Locate and identify every blood parasite.
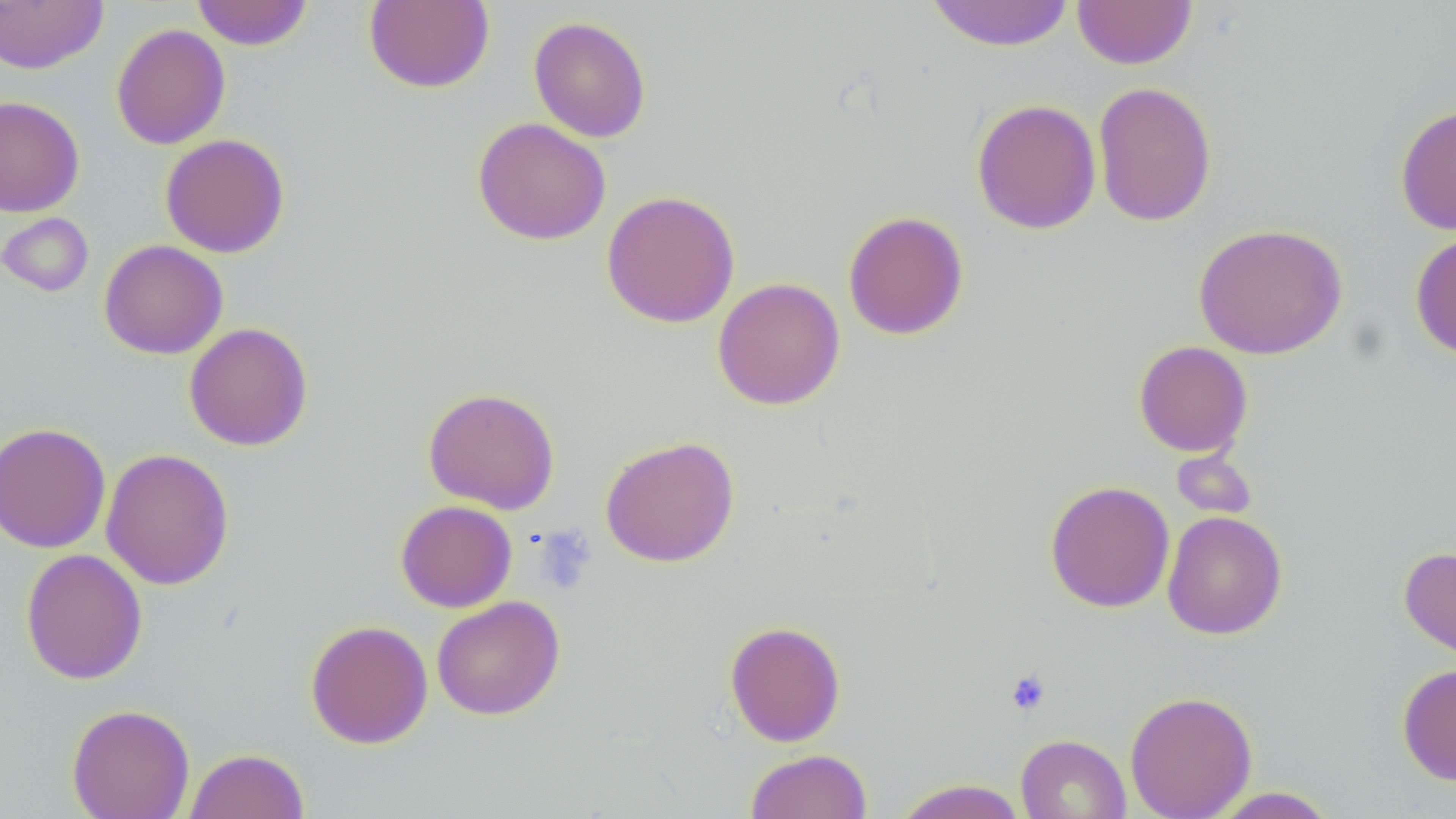

No blood parasites observed.

slide-level diagnosis = no evidence of blood parasites
field of view = single
stain = May-Grünwald-Giemsa
modality = optical microscopy
platelet locations = approximate bounding boxes as named x1/y1/x2/y2 corners in pixels: (x1=1005, y1=671, x2=1051, y2=715)
preparation = thin blood smear
uninfected red blood cell locations = approximate bounding boxes as named x1/y1/x2/y2 corners in pixels: (x1=191, y1=0, x2=313, y2=50), (x1=1072, y1=0, x2=1197, y2=70), (x1=0, y1=1, x2=108, y2=74), (x1=364, y1=1, x2=495, y2=93), (x1=926, y1=1, x2=1075, y2=52), (x1=529, y1=16, x2=652, y2=143), (x1=111, y1=23, x2=231, y2=150), (x1=1093, y1=81, x2=1217, y2=228), (x1=0, y1=95, x2=85, y2=217), (x1=971, y1=98, x2=1101, y2=235), (x1=1394, y1=103, x2=1456, y2=235), (x1=472, y1=117, x2=611, y2=246), (x1=160, y1=133, x2=290, y2=258), (x1=601, y1=190, x2=740, y2=328), (x1=842, y1=210, x2=969, y2=340), (x1=0, y1=213, x2=93, y2=297), (x1=1193, y1=223, x2=1347, y2=360), (x1=1410, y1=230, x2=1456, y2=360), (x1=99, y1=239, x2=228, y2=359), (x1=712, y1=277, x2=845, y2=410), (x1=184, y1=322, x2=313, y2=451), (x1=1133, y1=340, x2=1253, y2=457), (x1=422, y1=387, x2=560, y2=514), (x1=0, y1=422, x2=111, y2=553), (x1=600, y1=436, x2=739, y2=567), (x1=101, y1=448, x2=234, y2=590), (x1=1171, y1=449, x2=1258, y2=520), (x1=1044, y1=480, x2=1175, y2=613), (x1=395, y1=500, x2=517, y2=612), (x1=1162, y1=510, x2=1287, y2=639), (x1=1399, y1=545, x2=1456, y2=668), (x1=20, y1=548, x2=147, y2=685), (x1=431, y1=595, x2=565, y2=720), (x1=305, y1=619, x2=433, y2=749), (x1=724, y1=620, x2=846, y2=747), (x1=1397, y1=662, x2=1456, y2=787), (x1=1124, y1=690, x2=1257, y2=819), (x1=66, y1=703, x2=195, y2=819), (x1=1015, y1=734, x2=1131, y2=819), (x1=185, y1=748, x2=309, y2=819), (x1=745, y1=749, x2=872, y2=819), (x1=892, y1=779, x2=1029, y2=819), (x1=1207, y1=787, x2=1340, y2=818)
magnification = 1000x
image size = 1456×819 pixels